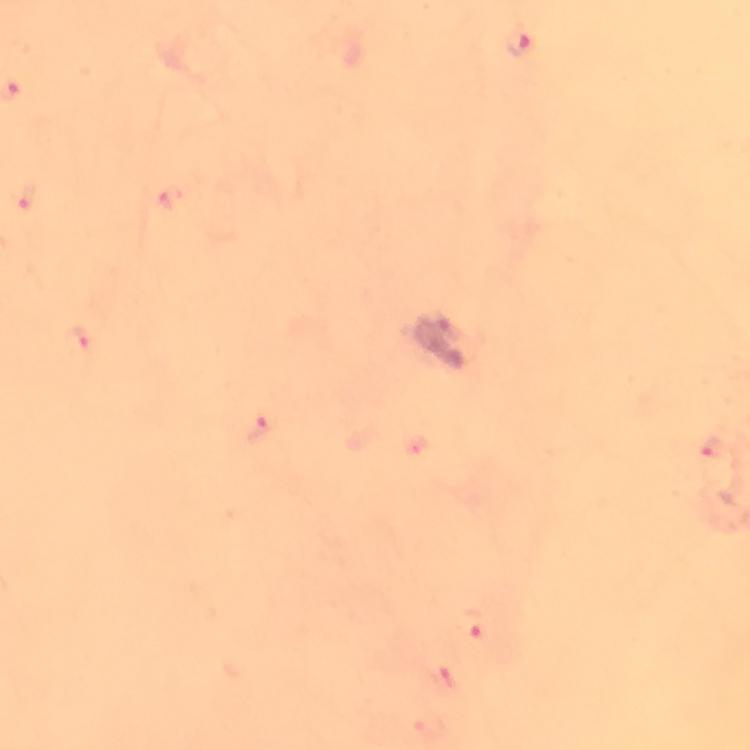
Approximate object centers, in pixels from the top-left corner.
Summary:
  - Malaria parasite locations: (x=519, y=46), (x=27, y=194), (x=82, y=339), (x=259, y=426), (x=711, y=448), (x=473, y=625), (x=443, y=681)
  - Context: from a diagnostic examination for malaria
  - Capture: smartphone mounted on the microscope
  - Immersion oil: used
  - Magnification: 100x
  - Stain: Giemsa
  - Cropped from: a single field of view
  - Preparation: thick blood film
  - Image size: 750×750 pixels